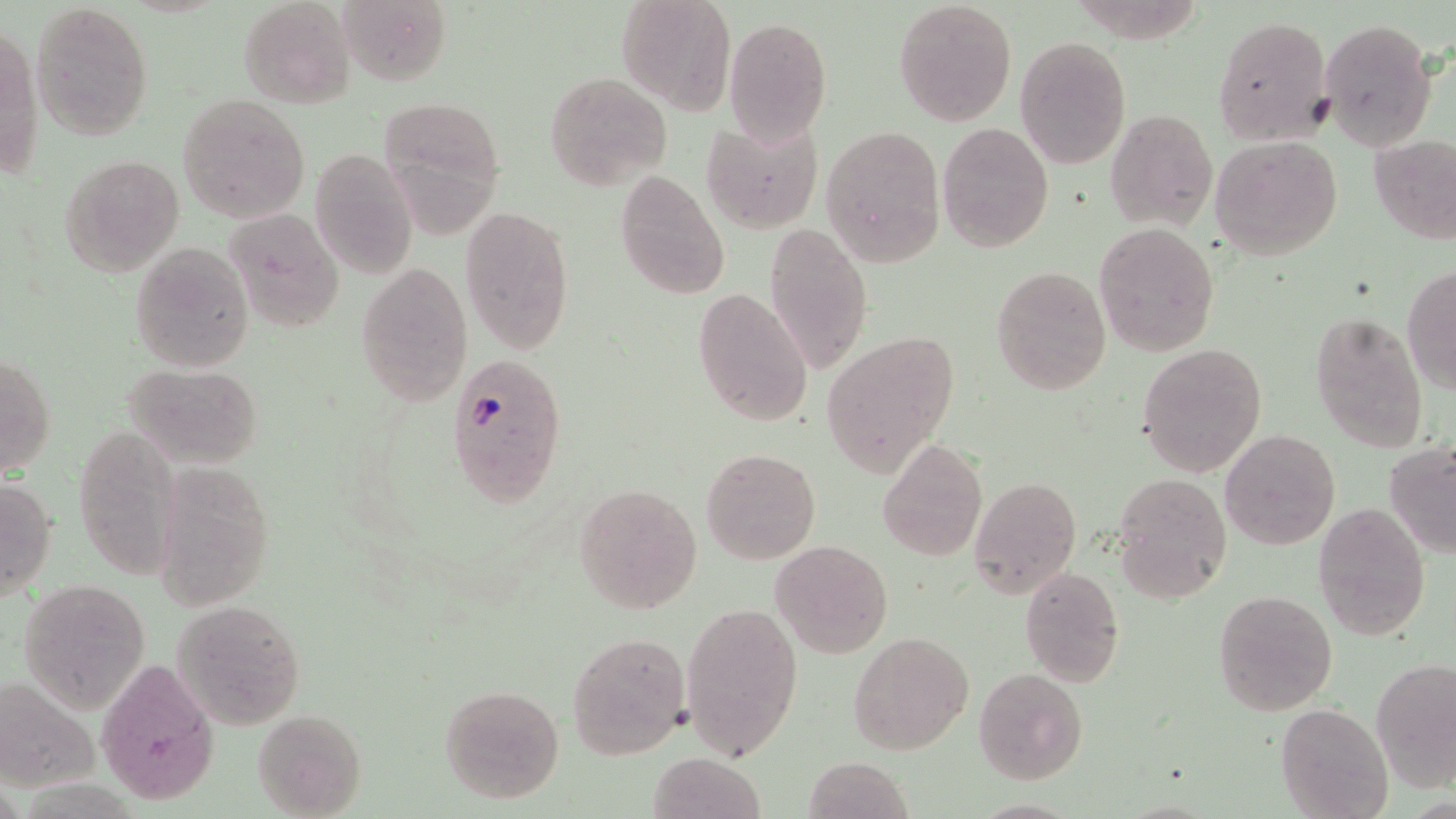 Approximate bounding boxes as (x1, y1, x2, y2) in pixels. Uninfected red blood cell locations: (239, 0, 356, 108), (338, 0, 450, 88), (617, 0, 736, 114), (32, 1, 154, 143), (893, 1, 1017, 125), (1213, 15, 1337, 145), (724, 17, 831, 144), (1319, 18, 1436, 150), (0, 20, 42, 182), (1015, 37, 1131, 168), (543, 72, 671, 188), (178, 94, 310, 224), (379, 99, 506, 232), (1104, 108, 1216, 232), (702, 119, 824, 234), (937, 121, 1052, 251), (821, 125, 946, 266), (1211, 134, 1343, 260), (1368, 134, 1456, 243), (308, 146, 420, 280), (59, 153, 183, 276), (613, 169, 730, 301), (460, 204, 576, 354), (224, 209, 344, 331), (763, 222, 871, 376), (1094, 222, 1218, 356), (130, 242, 253, 373), (355, 260, 472, 405), (990, 264, 1111, 396), (1402, 266, 1456, 395), (693, 287, 814, 427), (1309, 311, 1430, 454), (822, 329, 959, 475), (1137, 344, 1267, 477), (1, 352, 55, 479), (124, 361, 263, 469), (73, 423, 182, 584), (1220, 429, 1340, 549), (878, 439, 987, 561), (1384, 440, 1456, 559), (700, 447, 820, 564), (151, 461, 274, 612), (1113, 473, 1231, 603), (969, 475, 1080, 600), (1, 476, 57, 601), (573, 481, 702, 616), (1314, 503, 1430, 641), (770, 540, 894, 658), (1018, 567, 1124, 686), (18, 578, 150, 712), (1213, 589, 1337, 718), (173, 600, 306, 730), (680, 601, 804, 760), (566, 631, 690, 759), (848, 632, 973, 756), (97, 658, 219, 803), (1372, 658, 1456, 790), (974, 666, 1089, 783), (0, 678, 100, 792), (438, 683, 565, 804), (1274, 702, 1394, 819), (252, 709, 369, 818), (647, 752, 766, 819), (805, 755, 914, 819). Plasmodium falciparum-infected red blood cell locations: (447, 356, 567, 509). Slide-level diagnosis: Plasmodium falciparum. Image is 1456×819 pixels. May-Grünwald-Giemsa-stained preparation. One field of a larger specimen. Light microscopy. Thin blood smear. Captured at 1000x magnification.